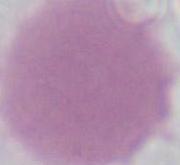
A red blood cell is shown. Photomicrograph. Captured at 1000x magnification.